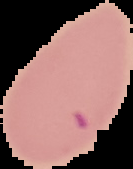

image size = 133×169 pixels
result = Plasmodium parasites identified
image type = segmented cell region on a black background
preparation = thin blood film